Locate every Plasmodium falciparum-infected red blood cell.
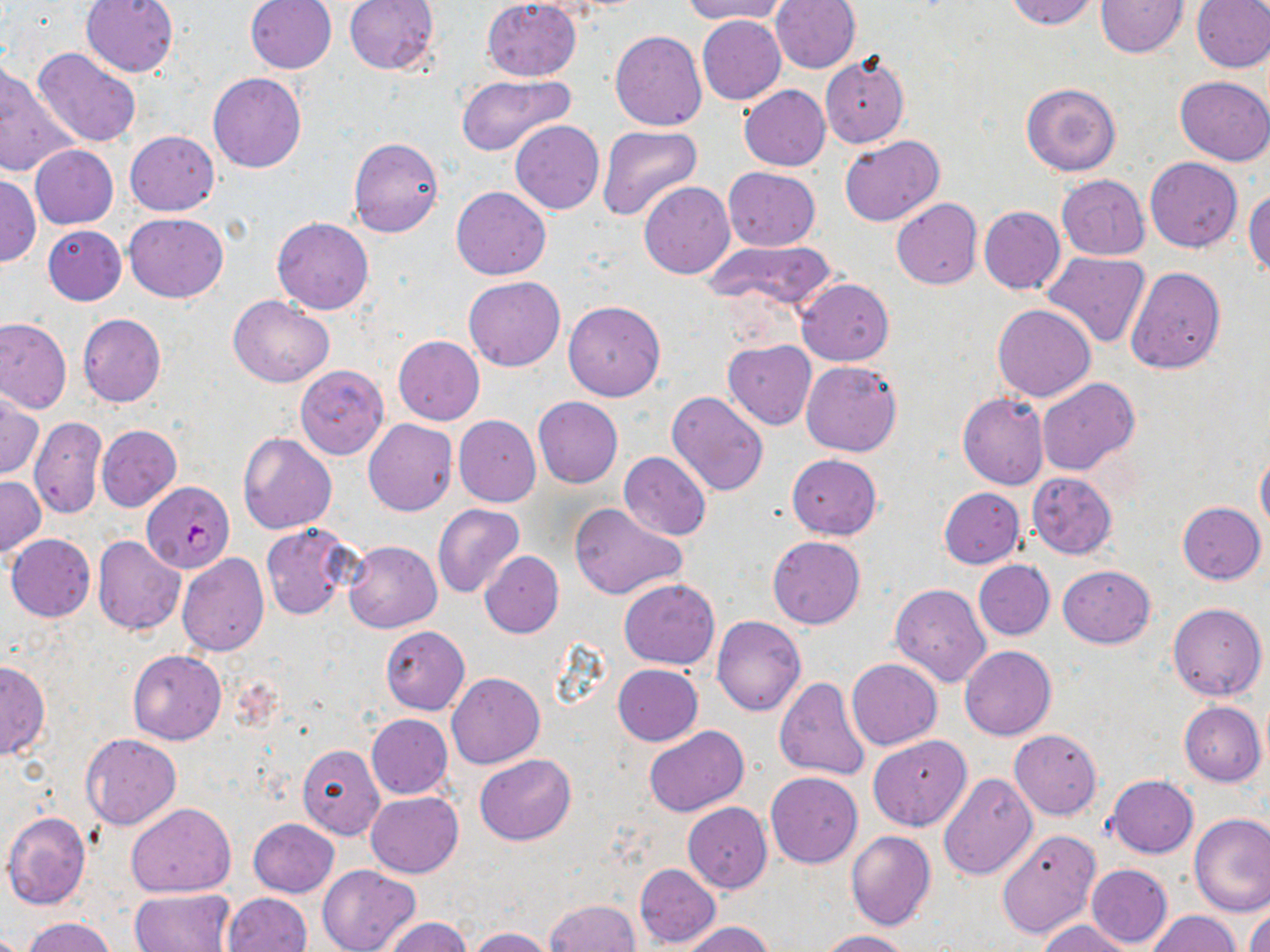

Approximate bounding boxes as [x1, y1, x2, y2] in pixels.
Plasmodium falciparum-infected red blood cells: [142, 481, 234, 572].

Summary:
  - Uninfected red blood cell locations: [80, 0, 178, 77], [245, 0, 337, 73], [344, 0, 439, 75], [481, 0, 581, 81], [680, 0, 791, 24], [771, 0, 861, 73], [1004, 0, 1099, 29], [1095, 0, 1187, 57], [1191, 0, 1270, 72], [698, 15, 786, 105], [610, 30, 707, 131], [33, 48, 142, 151], [820, 52, 909, 147], [0, 66, 81, 178], [208, 73, 306, 173], [454, 74, 573, 155], [1174, 76, 1270, 165], [1022, 83, 1121, 176], [740, 84, 830, 171], [511, 120, 603, 214], [597, 125, 702, 222], [125, 131, 219, 216], [839, 135, 945, 227], [348, 137, 444, 237], [30, 146, 117, 228], [1145, 157, 1243, 251], [724, 168, 820, 251], [1, 174, 40, 267], [1057, 175, 1149, 260], [639, 182, 735, 279], [450, 186, 552, 280], [1244, 186, 1270, 276], [891, 198, 983, 289], [978, 206, 1065, 294], [124, 213, 228, 302], [272, 217, 374, 314], [42, 225, 126, 305], [705, 238, 838, 312], [1043, 251, 1150, 348], [1125, 267, 1225, 373], [464, 275, 565, 371], [797, 278, 894, 366], [228, 295, 334, 387], [563, 300, 666, 402], [992, 303, 1096, 402], [78, 313, 166, 407], [0, 317, 71, 414], [393, 335, 485, 425], [723, 340, 817, 430], [801, 360, 901, 457], [294, 365, 388, 460], [1036, 377, 1140, 475], [667, 391, 769, 496], [1, 393, 42, 482], [958, 393, 1048, 490], [533, 396, 622, 488], [453, 415, 540, 506], [30, 417, 108, 519], [363, 418, 457, 516], [97, 425, 181, 511], [238, 431, 336, 534], [1256, 448, 1270, 535], [619, 452, 710, 540], [786, 453, 882, 539], [1026, 472, 1117, 559], [0, 476, 45, 558], [939, 488, 1024, 568], [569, 501, 687, 600], [1178, 501, 1266, 584], [433, 504, 526, 599], [261, 523, 355, 620], [6, 534, 96, 621], [93, 535, 184, 634], [767, 536, 866, 629], [344, 540, 441, 633], [480, 550, 563, 637], [176, 552, 269, 655], [973, 559, 1054, 641], [1057, 564, 1156, 648], [619, 579, 719, 669], [890, 584, 991, 687], [1168, 602, 1266, 701], [712, 615, 806, 716], [381, 627, 469, 714], [960, 646, 1057, 740], [128, 650, 227, 744], [846, 658, 942, 750], [0, 660, 50, 760], [612, 664, 703, 745], [447, 672, 545, 769], [773, 677, 871, 782], [1180, 701, 1266, 786], [366, 714, 452, 799], [643, 726, 749, 817], [1009, 729, 1102, 819], [81, 733, 182, 829], [867, 734, 972, 831], [296, 743, 385, 839], [475, 754, 578, 845], [766, 772, 863, 868], [938, 772, 1038, 880], [1107, 775, 1198, 857], [366, 792, 463, 878], [126, 802, 235, 897], [683, 803, 772, 892], [3, 812, 92, 909], [1189, 813, 1270, 916], [248, 818, 338, 898], [994, 828, 1101, 940], [846, 831, 937, 931], [635, 863, 721, 948], [317, 864, 419, 952], [1086, 864, 1173, 948], [131, 888, 234, 951], [225, 892, 312, 952], [547, 900, 640, 952], [1246, 905, 1270, 952], [1147, 911, 1241, 952], [23, 916, 116, 952], [381, 916, 471, 952], [1035, 919, 1134, 952], [680, 921, 775, 952], [469, 927, 555, 952], [816, 929, 913, 951]
  - Slide-level diagnosis: Plasmodium falciparum
  - Stain: May-Grünwald-Giemsa
  - Magnification: 1000x
  - Image size: 1270×952 pixels
  - Preparation: thin blood smear
  - Field of view: single
  - Modality: light microscopy